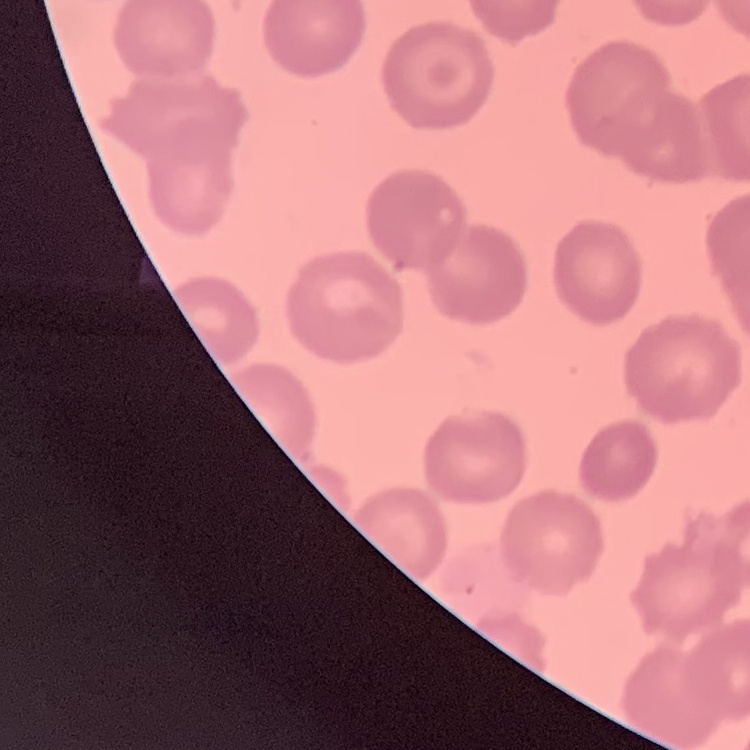

erythrocyte_morphology: no rouleaux formation
preparation: thin peripheral smear
stain: Field's or Giemsa
image_type: one tile cut from a larger photomicrograph